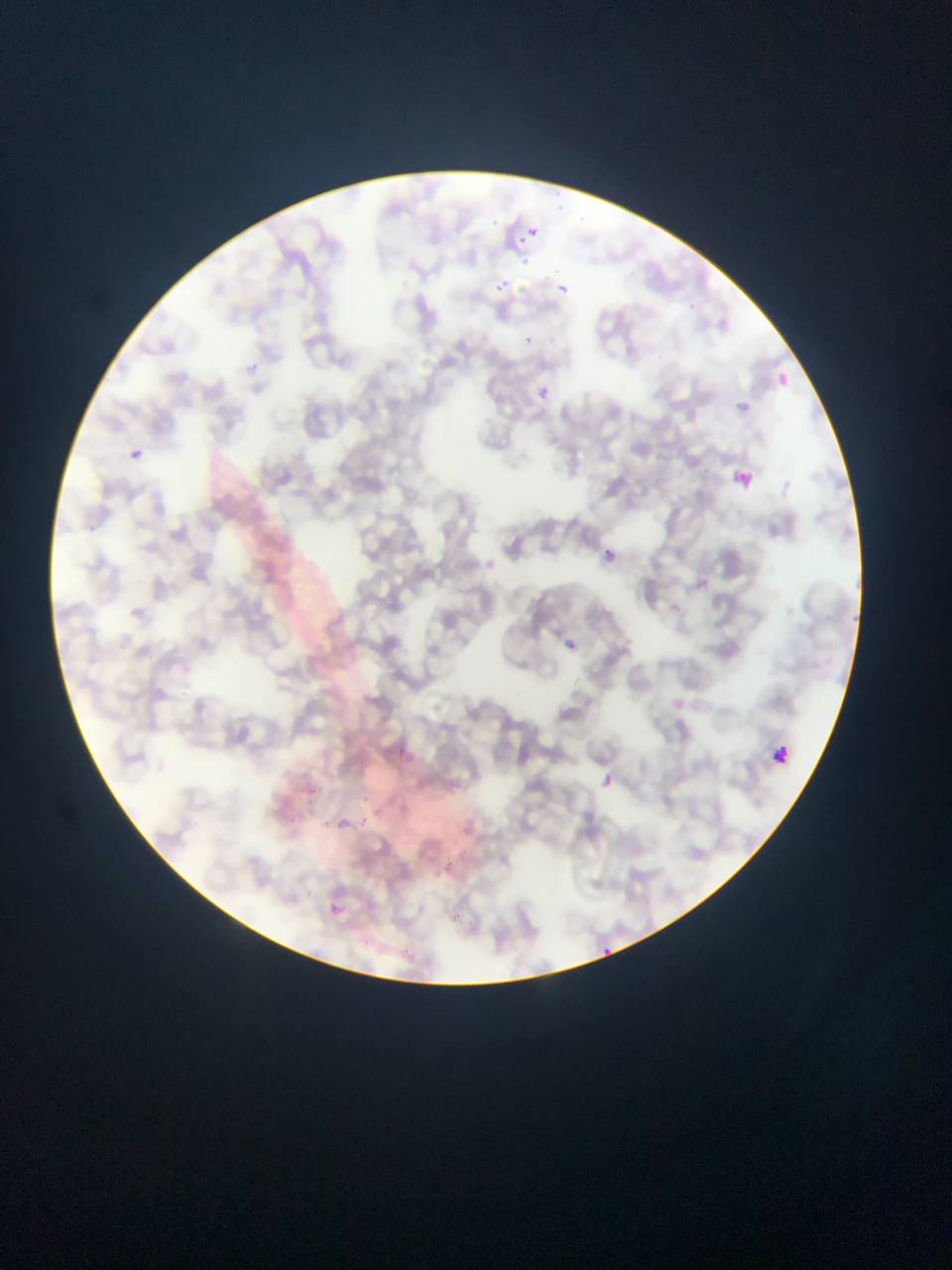
country = Ghana
leukocyte locations = approximate bounding boxes as [left, top, right, bottom] in pixels: [767, 738, 795, 765]
image size = 952×1270 pixels
capture = mobile-phone photograph through a microscope
preparation = thin blood smear
field of view = single
Plasmodium parasite locations = approximate bounding boxes as [left, top, right, bottom] in pixels: [490, 215, 498, 222], [528, 224, 545, 238], [518, 233, 524, 252], [486, 273, 516, 296], [545, 275, 578, 305], [523, 334, 536, 347], [776, 368, 811, 404], [532, 384, 563, 402], [730, 391, 768, 427], [129, 447, 144, 460], [733, 468, 764, 493], [595, 533, 640, 581], [130, 606, 144, 617], [561, 631, 595, 659], [597, 771, 619, 789], [330, 809, 356, 832], [359, 818, 368, 827], [327, 903, 346, 926], [599, 942, 621, 966]